Locate every blood parasite and identify its species.
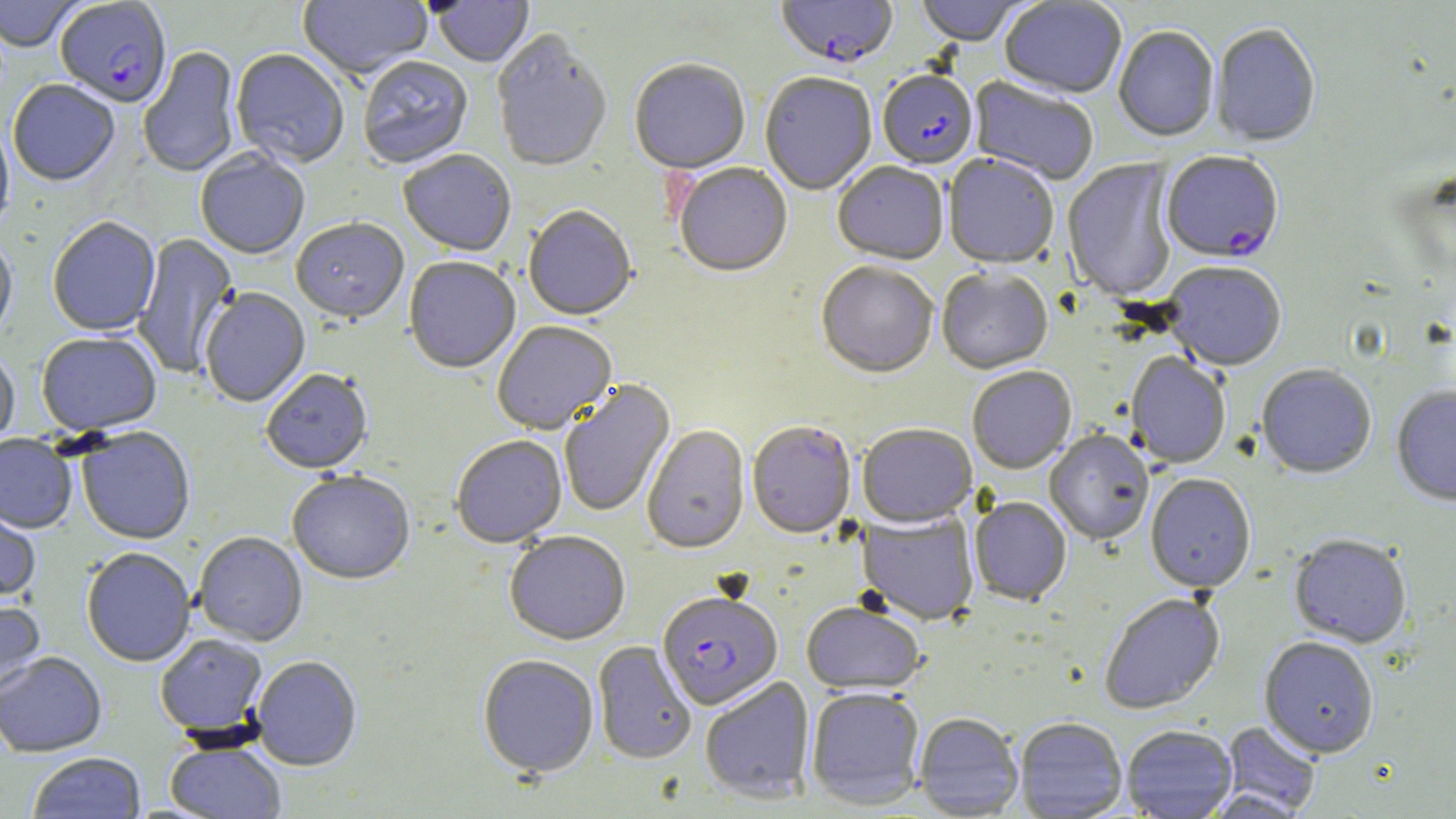

Approximate bounding boxes as [x1, y1, x2, y2] in pixels.
Plasmodium falciparum-infected red blood cells: [55, 1, 172, 110], [775, 1, 898, 71], [877, 72, 978, 171], [1161, 153, 1284, 266], [658, 593, 783, 712].
No Plasmodium ovale, Plasmodium malariae, Plasmodium vivax, Babesia divergens, or Trypanosoma brucei observed.

Uninfected red blood cell locations: [0, 0, 84, 54], [297, 0, 432, 82], [432, 0, 534, 68], [915, 0, 1033, 48], [999, 0, 1127, 100], [1210, 25, 1321, 149], [1113, 28, 1219, 144], [492, 32, 613, 175], [138, 47, 242, 180], [230, 51, 349, 170], [358, 57, 474, 170], [630, 62, 750, 177], [760, 74, 876, 197], [968, 77, 1099, 186], [8, 81, 120, 188], [0, 123, 15, 235], [195, 151, 310, 261], [399, 151, 517, 258], [943, 155, 1059, 270], [1062, 159, 1179, 304], [832, 163, 948, 267], [674, 164, 792, 279], [523, 207, 637, 323], [47, 218, 161, 337], [291, 220, 409, 327], [133, 232, 239, 378], [0, 237, 17, 348], [404, 258, 521, 375], [1163, 263, 1286, 373], [816, 264, 938, 381], [937, 270, 1053, 375], [200, 289, 310, 408], [492, 323, 617, 437], [36, 334, 162, 437], [0, 348, 20, 454], [1125, 353, 1231, 470], [1256, 366, 1376, 481], [967, 368, 1077, 475], [261, 371, 374, 477], [559, 380, 676, 518], [1392, 387, 1456, 508], [747, 423, 856, 540], [857, 424, 977, 530], [642, 426, 751, 556], [77, 427, 195, 546], [1044, 431, 1154, 546], [0, 435, 77, 535], [451, 437, 567, 550], [287, 473, 415, 587], [1145, 475, 1256, 595], [969, 498, 1072, 606], [0, 503, 41, 605], [857, 511, 980, 626], [505, 532, 630, 647], [193, 533, 308, 648], [1289, 537, 1411, 650], [81, 549, 196, 668], [1099, 594, 1225, 715], [0, 600, 46, 702], [802, 603, 926, 696], [155, 635, 270, 740], [1258, 639, 1379, 760], [592, 642, 697, 765], [0, 653, 107, 759], [478, 656, 599, 779], [251, 657, 362, 772], [699, 677, 816, 804], [806, 689, 925, 810], [914, 713, 1023, 818], [1015, 719, 1127, 818], [1221, 722, 1322, 816], [1121, 727, 1237, 818], [165, 742, 287, 818], [27, 753, 147, 819]. Slide-level diagnosis: Plasmodium falciparum. Thin blood film. Light microscopy. Single field of view. Image is 1456×819 pixels. May-Grünwald-Giemsa-stained preparation. 1000x magnification.